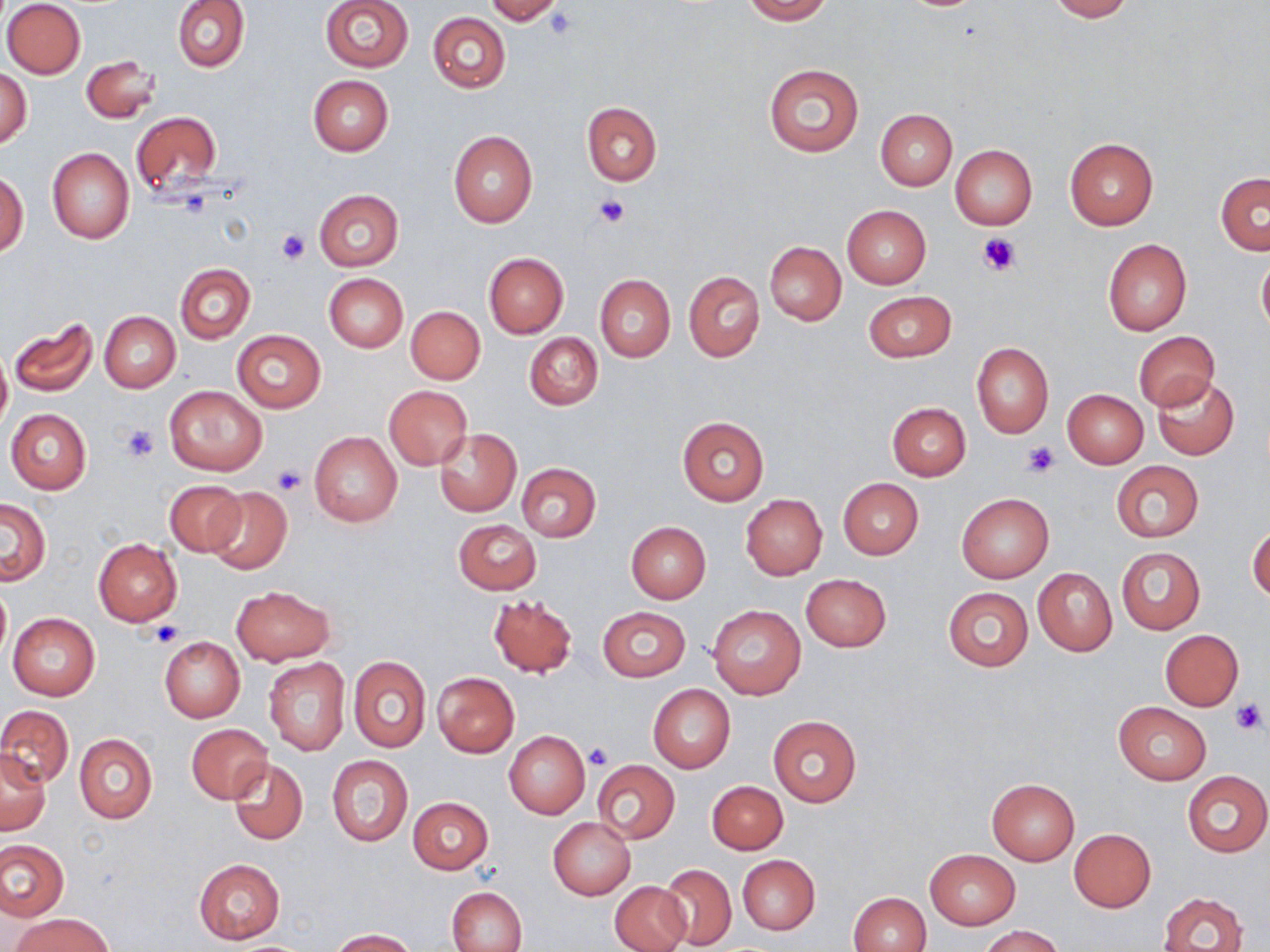 Approximate bounding boxes as (x1, y1, x2, y2) in pixels. Uninfected red blood cell locations: (172, 0, 249, 72), (321, 0, 413, 73), (484, 0, 564, 25), (742, 0, 833, 23), (1043, 0, 1135, 21), (2, 1, 85, 79), (427, 12, 510, 93), (81, 55, 160, 123), (763, 64, 864, 157), (0, 68, 32, 147), (308, 76, 393, 155), (582, 102, 661, 185), (876, 109, 957, 189), (130, 111, 223, 200), (448, 131, 537, 228), (1064, 139, 1158, 230), (949, 144, 1037, 229), (47, 147, 134, 243), (0, 171, 28, 257), (1215, 172, 1270, 255), (313, 189, 404, 270), (841, 205, 931, 288), (1102, 238, 1191, 335), (764, 241, 845, 325), (483, 252, 569, 337), (1256, 254, 1270, 339), (175, 264, 256, 343), (684, 271, 765, 361), (324, 274, 408, 352), (595, 275, 676, 363), (863, 291, 956, 362), (407, 307, 485, 384), (99, 311, 180, 391), (7, 317, 97, 398), (231, 329, 327, 412), (1133, 330, 1219, 410), (524, 333, 603, 410), (972, 343, 1054, 437), (0, 348, 12, 436), (1151, 374, 1239, 462), (164, 385, 268, 476), (384, 385, 472, 468), (1062, 389, 1148, 468), (886, 402, 970, 481), (5, 409, 92, 494), (677, 416, 770, 505), (434, 428, 522, 517), (309, 431, 402, 527), (1111, 460, 1205, 543), (517, 463, 602, 542), (838, 478, 923, 559), (164, 479, 246, 556), (205, 488, 292, 572), (956, 493, 1054, 582), (740, 495, 827, 579), (1, 498, 51, 585), (453, 519, 541, 594), (626, 522, 711, 603), (1248, 522, 1269, 605), (93, 537, 182, 626), (1116, 547, 1204, 634), (1033, 568, 1117, 656), (800, 573, 891, 651), (0, 582, 10, 661), (231, 585, 334, 664), (942, 586, 1033, 671), (487, 595, 577, 678), (708, 605, 807, 699), (597, 606, 691, 681), (7, 613, 100, 700), (1161, 630, 1244, 710), (159, 636, 245, 722), (349, 655, 431, 753), (264, 657, 350, 755), (432, 672, 519, 757), (648, 684, 735, 773), (1114, 702, 1211, 785), (0, 704, 74, 789), (767, 716, 861, 807), (187, 724, 271, 803), (504, 731, 590, 819), (75, 733, 157, 824), (0, 751, 51, 835), (326, 754, 412, 847), (229, 759, 308, 846), (592, 760, 681, 846), (1183, 771, 1269, 856), (986, 778, 1079, 864), (707, 780, 788, 854), (408, 797, 493, 874), (548, 818, 635, 898), (1069, 828, 1156, 911), (0, 840, 68, 921), (926, 849, 1020, 928), (737, 855, 820, 934), (194, 859, 284, 943), (660, 864, 736, 949), (610, 880, 691, 952), (448, 887, 528, 952), (1158, 891, 1249, 952), (848, 892, 931, 952), (11, 913, 114, 952), (979, 925, 1064, 952), (328, 929, 419, 951). Platelet locations: (545, 8, 578, 39), (595, 195, 630, 226), (276, 230, 310, 265), (976, 231, 1022, 278), (121, 423, 159, 461), (1023, 441, 1059, 478), (271, 464, 307, 495), (151, 622, 182, 647), (1232, 699, 1267, 734), (584, 744, 613, 771). Slide-level diagnosis: negative for blood parasites. Thin blood smear. Captured at 1000x magnification. Single field of view. Light microscopy. Image is 1270×952 pixels. May-Grünwald-Giemsa-stained preparation.